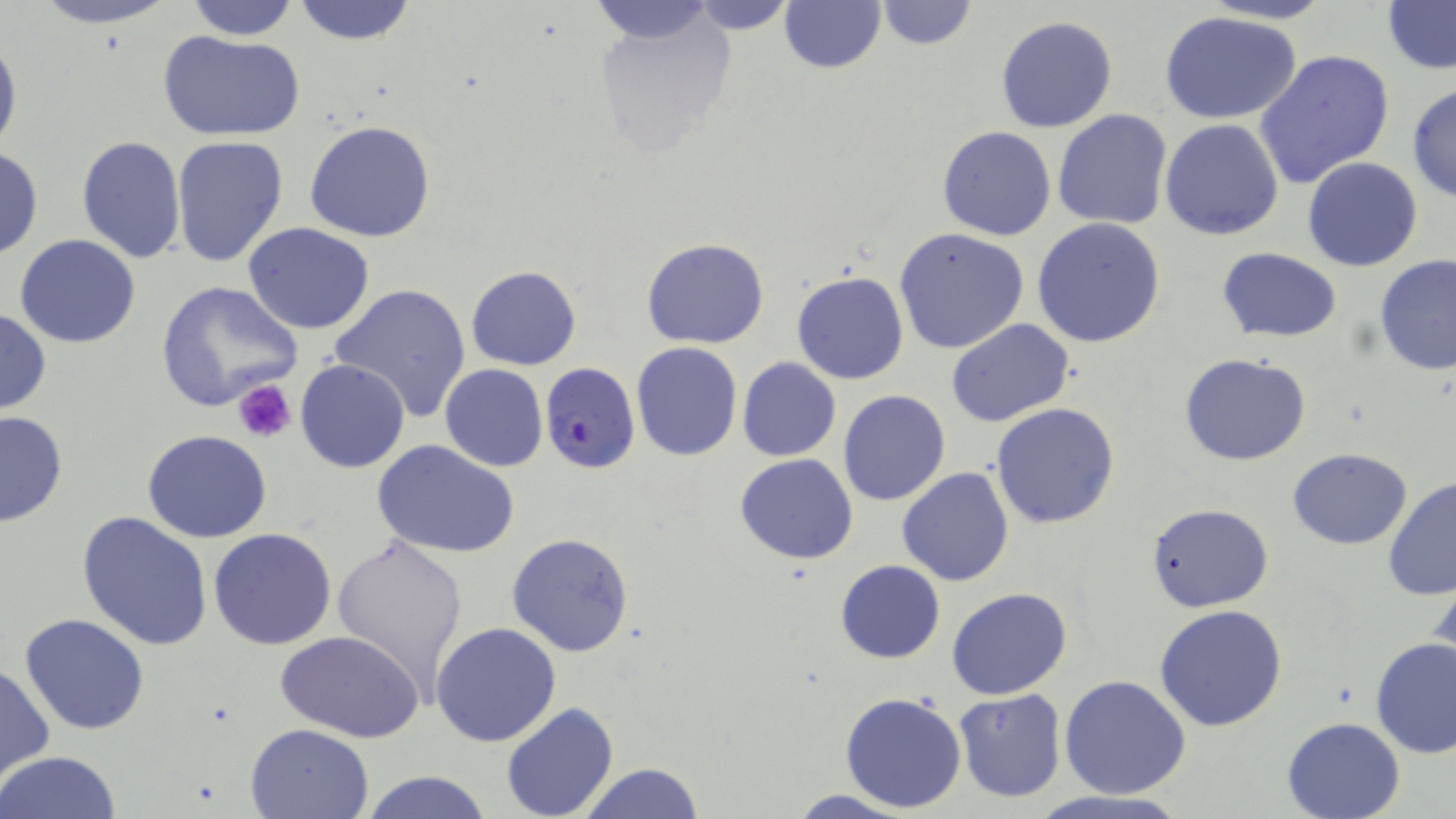

Approximate bounding boxes as named x1/y1/x2/y2 corners in pixels. Platelet locations: (x1=232, y1=380, x2=296, y2=441). Uninfected red blood cell locations: (x1=27, y1=0, x2=180, y2=29), (x1=181, y1=0, x2=303, y2=41), (x1=586, y1=0, x2=720, y2=48), (x1=683, y1=0, x2=801, y2=33), (x1=873, y1=0, x2=978, y2=49), (x1=1194, y1=0, x2=1339, y2=25), (x1=291, y1=1, x2=419, y2=47), (x1=1381, y1=1, x2=1456, y2=74), (x1=778, y1=2, x2=886, y2=75), (x1=1160, y1=10, x2=1304, y2=124), (x1=591, y1=12, x2=740, y2=158), (x1=994, y1=16, x2=1117, y2=134), (x1=159, y1=30, x2=305, y2=142), (x1=0, y1=32, x2=21, y2=160), (x1=1254, y1=50, x2=1395, y2=189), (x1=1406, y1=82, x2=1456, y2=202), (x1=1052, y1=108, x2=1172, y2=231), (x1=1160, y1=118, x2=1286, y2=240), (x1=305, y1=121, x2=436, y2=242), (x1=937, y1=126, x2=1055, y2=241), (x1=75, y1=134, x2=187, y2=264), (x1=170, y1=134, x2=290, y2=268), (x1=0, y1=148, x2=43, y2=259), (x1=1302, y1=157, x2=1424, y2=271), (x1=1032, y1=218, x2=1166, y2=350), (x1=243, y1=222, x2=376, y2=334), (x1=894, y1=228, x2=1029, y2=354), (x1=14, y1=234, x2=142, y2=348), (x1=642, y1=238, x2=768, y2=349), (x1=1218, y1=248, x2=1342, y2=341), (x1=1376, y1=253, x2=1456, y2=375), (x1=466, y1=266, x2=582, y2=371), (x1=792, y1=271, x2=908, y2=386), (x1=155, y1=279, x2=302, y2=412), (x1=329, y1=282, x2=473, y2=423), (x1=0, y1=306, x2=50, y2=417), (x1=947, y1=319, x2=1075, y2=426), (x1=631, y1=341, x2=742, y2=461), (x1=1179, y1=353, x2=1312, y2=466), (x1=736, y1=357, x2=841, y2=462), (x1=295, y1=358, x2=410, y2=473), (x1=440, y1=364, x2=548, y2=471), (x1=838, y1=390, x2=951, y2=506), (x1=989, y1=402, x2=1120, y2=529), (x1=0, y1=411, x2=69, y2=527), (x1=143, y1=430, x2=272, y2=543), (x1=374, y1=441, x2=518, y2=556), (x1=1286, y1=447, x2=1414, y2=548), (x1=734, y1=454, x2=858, y2=564), (x1=897, y1=466, x2=1013, y2=585), (x1=170, y1=473, x2=314, y2=630), (x1=1382, y1=476, x2=1456, y2=600), (x1=1148, y1=503, x2=1274, y2=612), (x1=77, y1=511, x2=213, y2=650), (x1=208, y1=527, x2=338, y2=649), (x1=331, y1=531, x2=471, y2=699), (x1=505, y1=532, x2=634, y2=658), (x1=836, y1=559, x2=946, y2=663), (x1=1428, y1=565, x2=1456, y2=676), (x1=947, y1=587, x2=1072, y2=699), (x1=1155, y1=604, x2=1288, y2=732), (x1=19, y1=613, x2=150, y2=735), (x1=431, y1=623, x2=562, y2=747), (x1=279, y1=631, x2=422, y2=743), (x1=1370, y1=637, x2=1456, y2=757), (x1=0, y1=663, x2=54, y2=782), (x1=1059, y1=674, x2=1191, y2=798), (x1=952, y1=689, x2=1067, y2=802), (x1=840, y1=691, x2=967, y2=811), (x1=500, y1=703, x2=618, y2=819), (x1=1279, y1=716, x2=1405, y2=819), (x1=246, y1=722, x2=375, y2=817), (x1=1, y1=751, x2=123, y2=819), (x1=577, y1=761, x2=705, y2=818), (x1=358, y1=771, x2=494, y2=819), (x1=782, y1=789, x2=922, y2=819), (x1=1026, y1=792, x2=1191, y2=819). Plasmodium falciparum-infected red blood cell locations: (x1=540, y1=362, x2=640, y2=474). Slide-level diagnosis: Plasmodium falciparum. Thin blood smear. May-Grünwald-Giemsa-stained preparation. 1000x magnification. Light microscopy. Image is 1456×819 pixels. One field of a larger specimen.